Locate and identify every blood parasite.
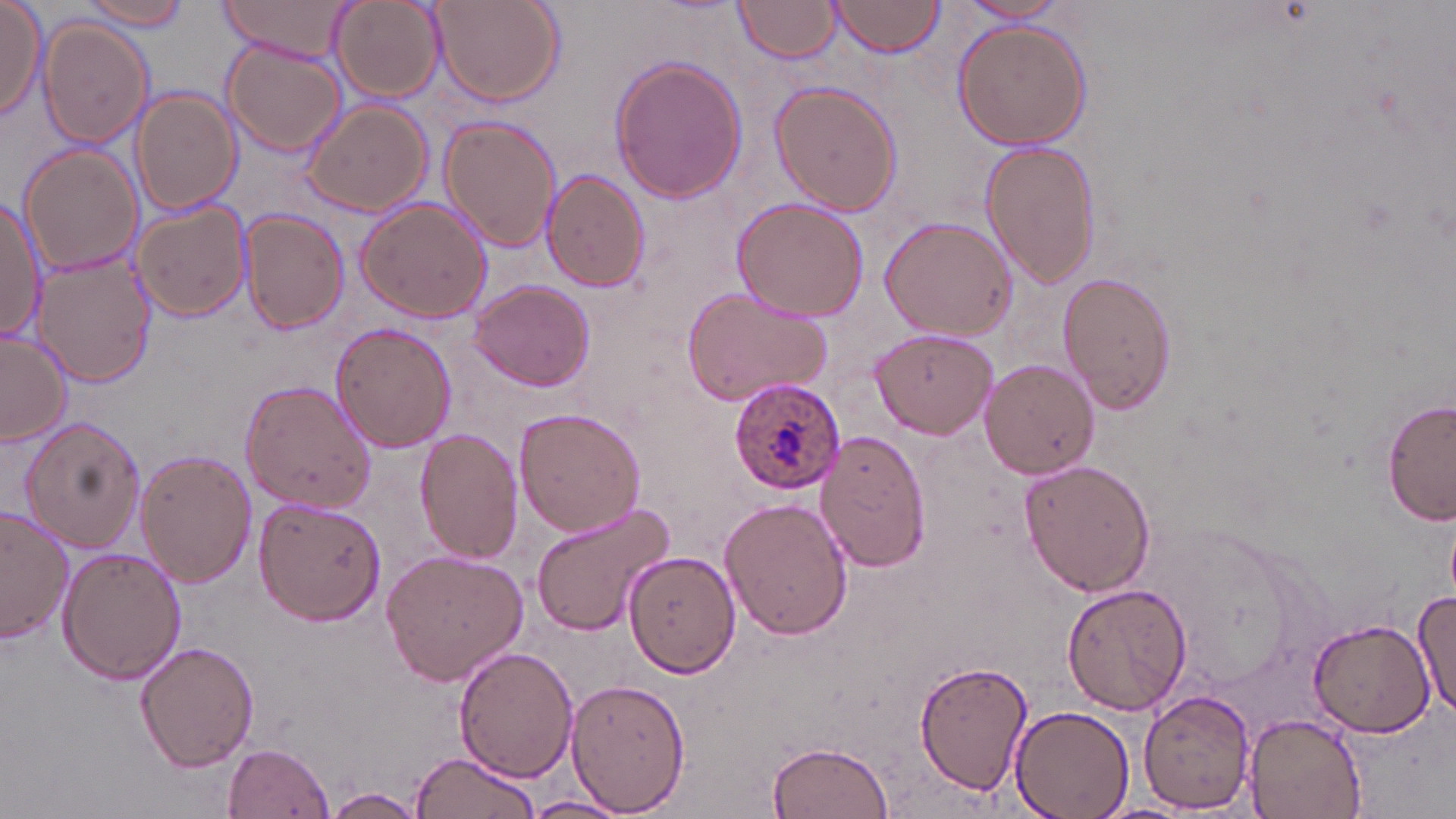

Approximate bounding boxes as [x1, y1, x2, y2] in pixels.
Plasmodium ovale-infected red blood cells: [730, 378, 844, 495].
No Plasmodium falciparum, Plasmodium malariae, Plasmodium vivax, Babesia divergens, or Trypanosoma brucei observed.

Uninfected red blood cell locations: [0, 0, 47, 118], [217, 0, 358, 64], [427, 0, 565, 108], [731, 0, 843, 63], [828, 0, 946, 58], [77, 1, 192, 31], [330, 1, 443, 101], [957, 1, 1073, 27], [952, 18, 1093, 151], [38, 20, 153, 147], [221, 42, 344, 156], [611, 54, 746, 203], [768, 80, 902, 216], [130, 88, 242, 214], [301, 100, 433, 217], [439, 115, 561, 253], [979, 138, 1102, 288], [21, 147, 141, 276], [542, 171, 648, 293], [0, 195, 45, 344], [729, 196, 868, 322], [356, 197, 491, 323], [132, 201, 251, 321], [240, 208, 350, 335], [878, 215, 1017, 339], [32, 253, 153, 388], [1057, 269, 1179, 415], [468, 279, 596, 392], [680, 285, 835, 407], [331, 321, 456, 452], [867, 327, 998, 438], [0, 329, 72, 447], [979, 359, 1100, 478], [237, 378, 375, 513], [1382, 397, 1455, 527], [513, 406, 646, 536], [18, 417, 145, 552], [415, 427, 524, 563], [816, 429, 933, 572], [137, 449, 257, 589], [1019, 459, 1155, 596], [253, 496, 385, 626], [720, 498, 852, 640], [529, 503, 677, 635], [0, 506, 74, 645], [56, 545, 186, 685], [604, 546, 742, 679], [380, 550, 528, 688], [1062, 581, 1192, 717], [1411, 587, 1456, 718], [1309, 617, 1440, 737], [135, 639, 257, 772], [455, 645, 579, 781], [915, 659, 1032, 795], [568, 674, 691, 813], [1138, 686, 1256, 812], [1009, 704, 1136, 819], [1242, 711, 1367, 817], [766, 740, 896, 817], [223, 742, 336, 819], [408, 751, 542, 819], [323, 787, 429, 817], [523, 794, 631, 819], [1085, 801, 1202, 819]. Slide-level diagnosis: Plasmodium ovale. Image is 1456×819 pixels. May-Grünwald-Giemsa-stained preparation. Thin blood film. Light microscopy. 1000x magnification. Single field of view.